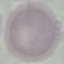 Malaria status: uninfected. Acquired by smartphone through the microscope eyepiece. Giemsa stain. Thin blood film. Cell patch, automatically extracted from a larger field of view and resized to 64 × 64 pixels.